Assess this cell for malaria.
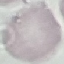

It is uninfected.

capture = smartphone through the microscope eyepiece
preparation = thin blood smear
image type = automatically extracted cell patch, resized to 64 × 64 pixels
stain = Giemsa